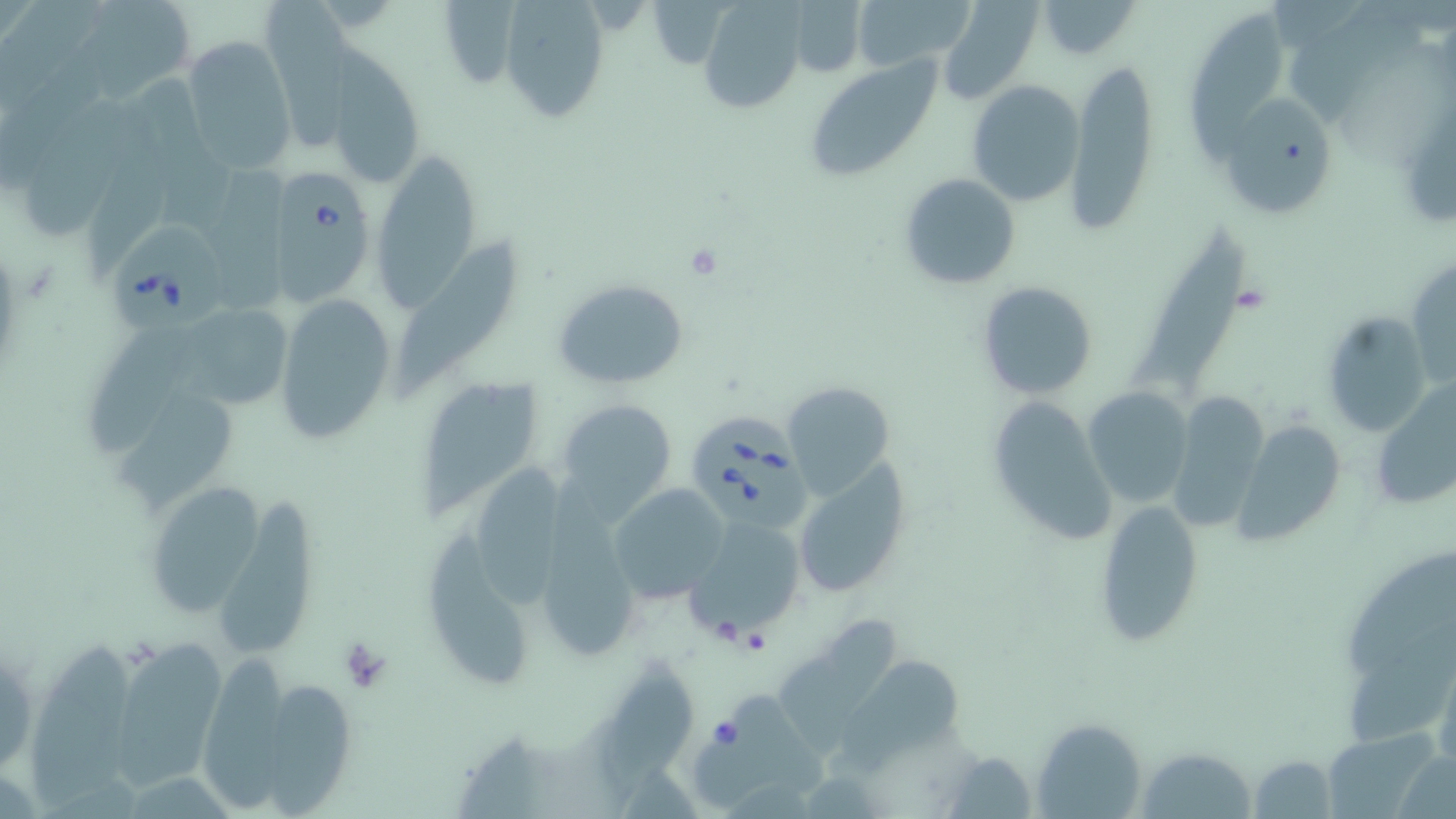

slide-level diagnosis = Babesia divergens
stain = May-Grünwald-Giemsa
uninfected red blood cell locations = approximate bounding boxes as [x1, y1, x2, y2] in pixels: [71, 0, 196, 104], [258, 0, 347, 151], [853, 0, 977, 72], [697, 1, 806, 115], [789, 1, 867, 78], [936, 1, 1044, 106], [1035, 1, 1142, 60], [499, 2, 612, 122], [1287, 5, 1429, 121], [1189, 9, 1287, 166], [181, 36, 295, 175], [321, 54, 427, 192], [805, 56, 945, 183], [1064, 59, 1160, 235], [968, 80, 1086, 205], [137, 84, 232, 229], [19, 95, 138, 241], [1223, 98, 1334, 211], [370, 148, 479, 312], [202, 160, 291, 304], [898, 172, 1022, 291], [1136, 223, 1253, 390], [392, 233, 516, 399], [1408, 257, 1456, 389], [553, 278, 689, 388], [977, 281, 1099, 400], [274, 292, 398, 443], [194, 311, 298, 411], [1321, 312, 1430, 438], [87, 325, 201, 457], [425, 376, 542, 524], [1372, 379, 1456, 515], [781, 381, 897, 501], [1082, 386, 1194, 508], [1170, 393, 1268, 529], [988, 394, 1115, 545], [113, 395, 236, 519], [554, 398, 678, 517], [1237, 420, 1348, 547], [478, 454, 569, 608], [791, 461, 911, 601], [144, 478, 266, 619], [608, 484, 730, 604], [217, 497, 315, 657], [1094, 500, 1203, 645], [683, 515, 807, 642], [535, 523, 642, 662], [428, 530, 531, 689], [778, 613, 897, 752], [101, 633, 230, 786], [27, 645, 145, 809], [1432, 651, 1456, 775], [207, 655, 292, 814], [604, 656, 701, 792], [842, 658, 960, 768], [263, 683, 361, 813], [688, 687, 828, 804], [1031, 718, 1148, 818], [1136, 747, 1257, 818], [1247, 754, 1339, 818]
platelet locations = approximate bounding boxes as [x1, y1, x2, y2] in pixels: [684, 242, 726, 282], [336, 637, 392, 691]
preparation = thin blood film
field of view = one of a larger specimen
magnification = 1000x
modality = light microscopy
Babesia divergens-infected red blood cell locations = approximate bounding boxes as [x1, y1, x2, y2] in pixels: [261, 166, 378, 303], [109, 215, 234, 336], [690, 412, 819, 526]
image size = 1456×819 pixels